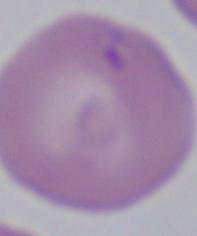

magnification: 1000x
modality: photomicrograph
identification: Babesia